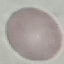

{
  "malaria_status": "uninfected",
  "capture": "smartphone camera at the microscope eyepiece",
  "preparation": "thin blood film",
  "stain": "Giemsa",
  "image_type": "automatically extracted cell patch, resized to 64 × 64 pixels"
}